Identify the cell.
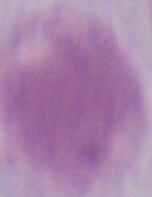
This is an erythrocyte.

Summary:
  - Modality: photomicrograph
  - Magnification: 1000x